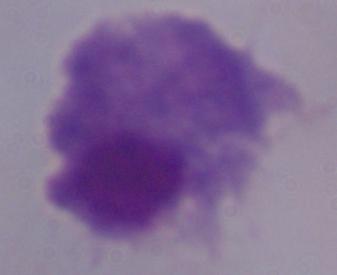
1000x magnification. A trichomonad is seen. Photomicrograph.